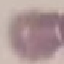
{
  "result": "negative for malaria parasites",
  "preparation": "thin blood film",
  "stain": "Giemsa",
  "image_type": "automatically extracted cell patch, resized to 64 × 64 pixels",
  "capture": "smartphone camera at the microscope eyepiece"
}